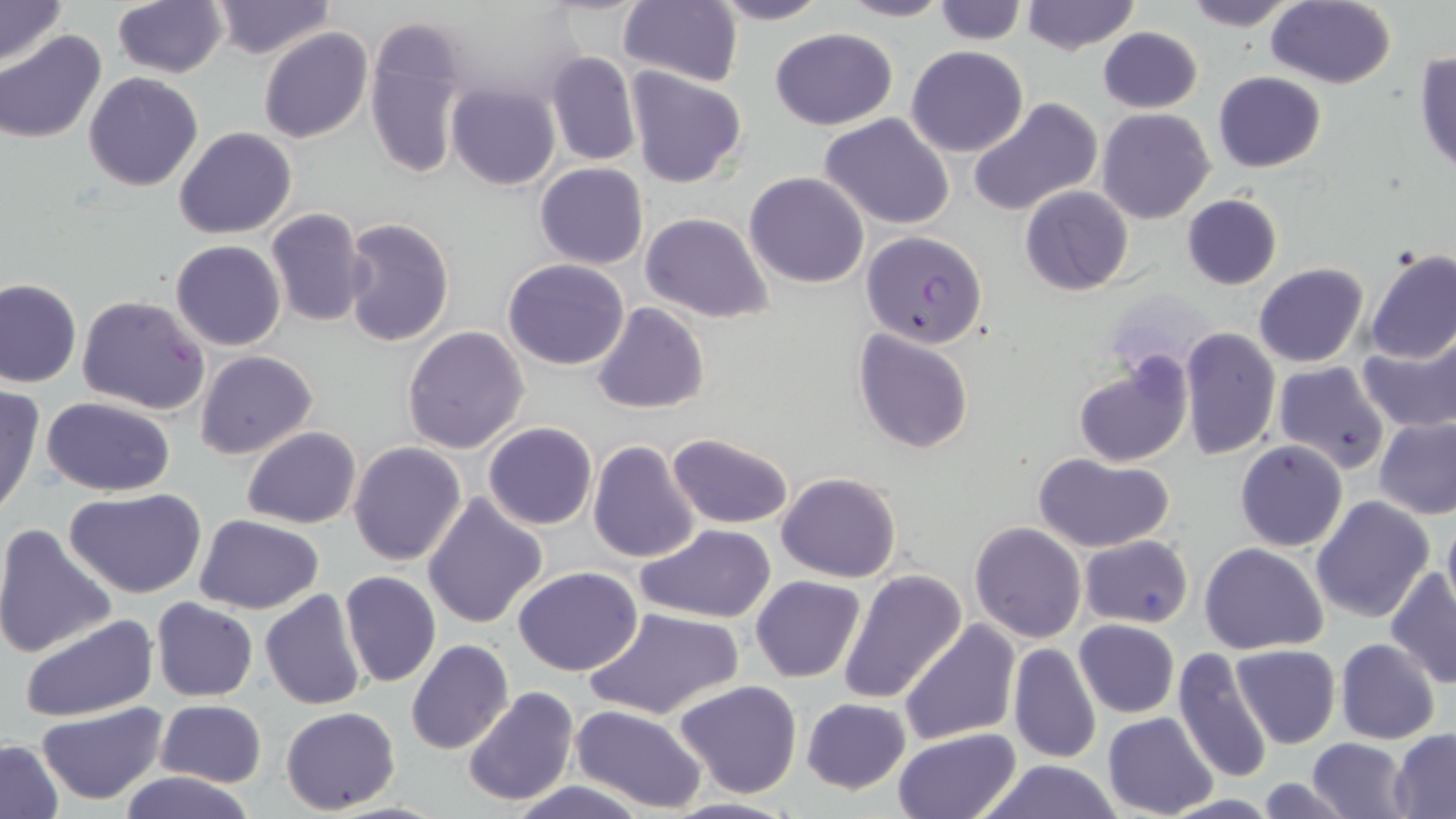
{
  "slide_level_diagnosis": "Plasmodium falciparum",
  "magnification": "1000x",
  "image_size": "1456×819 pixels",
  "uninfected_red_blood_cell_locations": "approximate bounding boxes as [x1, y1, x2, y2] in pixels: [0, 0, 68, 67], [209, 0, 335, 60], [618, 0, 743, 87], [709, 0, 832, 25], [837, 0, 952, 23], [933, 0, 1028, 45], [1019, 0, 1140, 54], [1180, 0, 1302, 30], [113, 1, 226, 77], [1266, 1, 1396, 88], [364, 20, 467, 182], [1098, 26, 1202, 113], [769, 27, 897, 129], [259, 28, 373, 145], [0, 30, 107, 144], [906, 45, 1029, 158], [564, 47, 700, 182], [1414, 49, 1456, 175], [546, 50, 641, 167], [624, 67, 748, 189], [1213, 71, 1326, 172], [82, 73, 203, 191], [447, 83, 560, 190], [968, 97, 1104, 217], [1097, 108, 1214, 224], [819, 113, 955, 229], [174, 127, 296, 240], [535, 162, 649, 269], [744, 172, 870, 289], [1020, 186, 1133, 295], [1182, 195, 1283, 290], [265, 208, 369, 327], [640, 211, 774, 323], [340, 216, 457, 348], [170, 240, 286, 351], [1365, 250, 1456, 364], [503, 258, 630, 370], [1254, 262, 1369, 367], [0, 277, 82, 388], [76, 294, 211, 416], [590, 302, 711, 416], [402, 324, 530, 453], [1179, 327, 1281, 463], [852, 328, 975, 455], [1357, 330, 1456, 433], [194, 350, 320, 461], [1070, 350, 1194, 470], [1272, 361, 1391, 475], [0, 384, 46, 519], [42, 398, 177, 496], [1374, 416, 1456, 519], [482, 422, 597, 531], [241, 427, 362, 528], [668, 431, 796, 529], [589, 439, 703, 565], [1235, 440, 1348, 552], [348, 442, 467, 567], [1032, 453, 1175, 553], [1272, 462, 1400, 607], [777, 471, 902, 583], [65, 488, 206, 599], [421, 492, 548, 630], [1311, 496, 1435, 624], [1441, 512, 1456, 619], [195, 514, 325, 613], [0, 521, 118, 660], [969, 522, 1086, 643], [637, 524, 777, 624], [1079, 535, 1194, 628], [1199, 542, 1329, 654], [513, 567, 642, 677], [836, 568, 969, 707], [1385, 568, 1456, 690], [339, 570, 441, 690], [751, 576, 866, 683], [260, 589, 370, 710], [151, 598, 258, 702], [586, 605, 744, 721], [18, 613, 158, 723], [1074, 619, 1178, 718], [898, 620, 1020, 747], [406, 638, 514, 756], [1335, 638, 1440, 744], [1007, 643, 1102, 764], [1233, 645, 1339, 747], [1171, 648, 1274, 784], [673, 679, 803, 800], [461, 685, 580, 808], [156, 698, 267, 788], [801, 698, 911, 793], [36, 702, 169, 804], [569, 704, 708, 814], [280, 707, 401, 813], [1102, 712, 1218, 819], [891, 727, 1022, 819], [1390, 731, 1456, 816], [1306, 738, 1412, 819], [0, 739, 64, 817], [971, 759, 1127, 819], [118, 770, 257, 819], [1255, 775, 1354, 818], [504, 779, 649, 818], [660, 796, 800, 818]",
  "stain": "May-Grünwald-Giemsa",
  "plasmodium_falciparum_infected_red_blood_cell_locations": "approximate bounding boxes as [x1, y1, x2, y2] in pixels: [863, 229, 988, 346]",
  "field_of_view": "one of a larger specimen",
  "preparation": "thin blood film",
  "modality": "optical microscopy"
}